Classify this cell by malaria status.
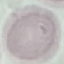

It is uninfected.

{
  "capture": "smartphone through the microscope eyepiece",
  "preparation": "thin blood film",
  "stain": "Giemsa",
  "image_type": "automatically extracted cell patch, resized to 64 × 64 pixels"
}